Point out every malaria parasite and every leukocyte.
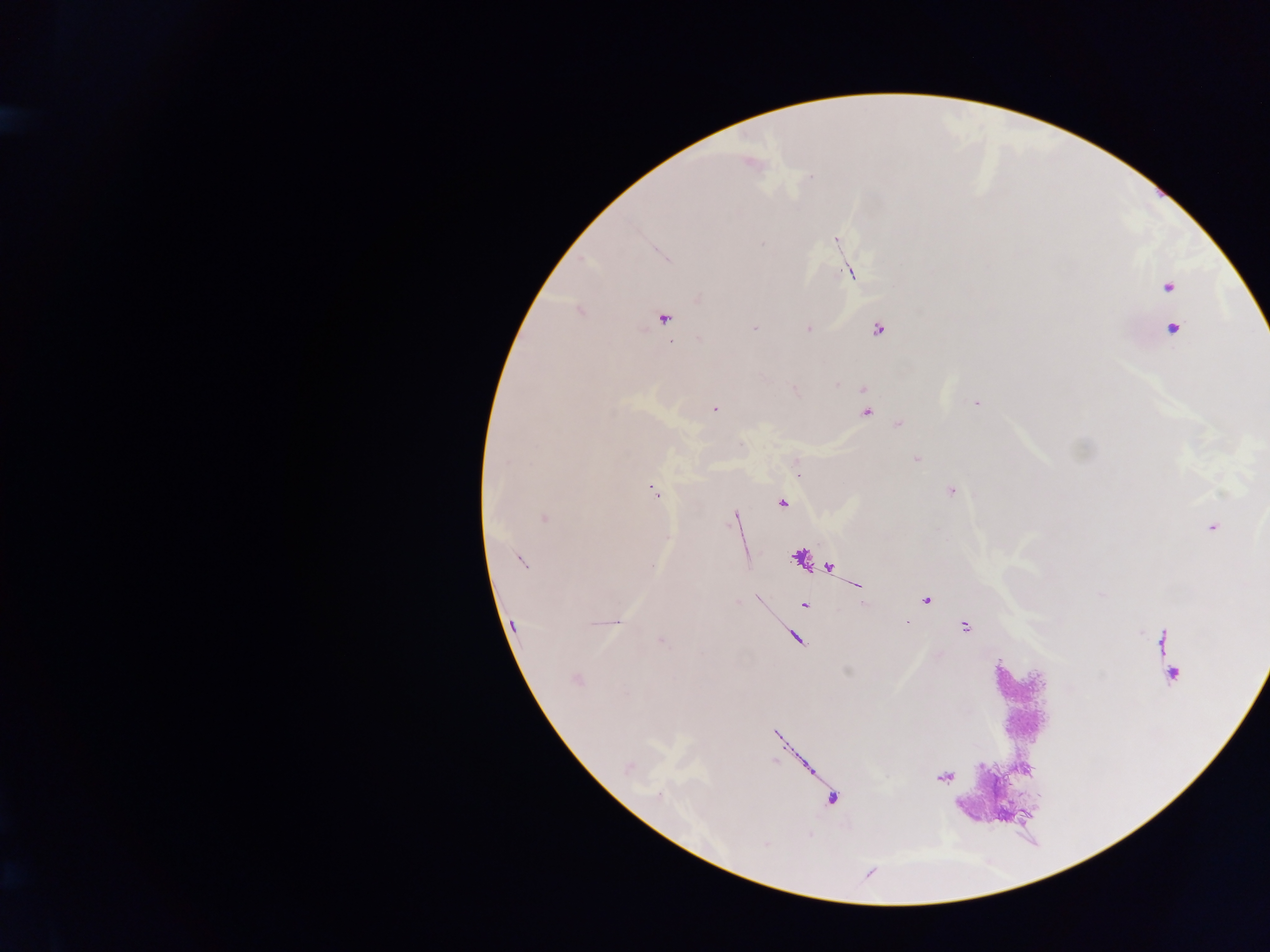
Approximate centers as (x, y) in pixels.
Malaria parasites: (835, 240), (762, 243), (849, 273), (698, 299), (665, 318), (754, 327), (808, 329), (878, 330), (698, 338), (977, 403), (714, 409), (866, 413), (899, 424), (916, 459), (507, 462), (950, 491), (653, 492), (781, 503), (544, 517), (734, 517), (1212, 528), (522, 561), (926, 599), (804, 606), (906, 621), (617, 622), (513, 624), (965, 627), (661, 640), (577, 680), (659, 795), (765, 843).
Leukocytes: (1169, 288), (1176, 326).

Summary:
  - Preparation: thick blood film
  - Image size: 1270×952 pixels
  - Capture: mobile-phone photograph through a microscope
  - Country: Ghana
  - Field of view: single